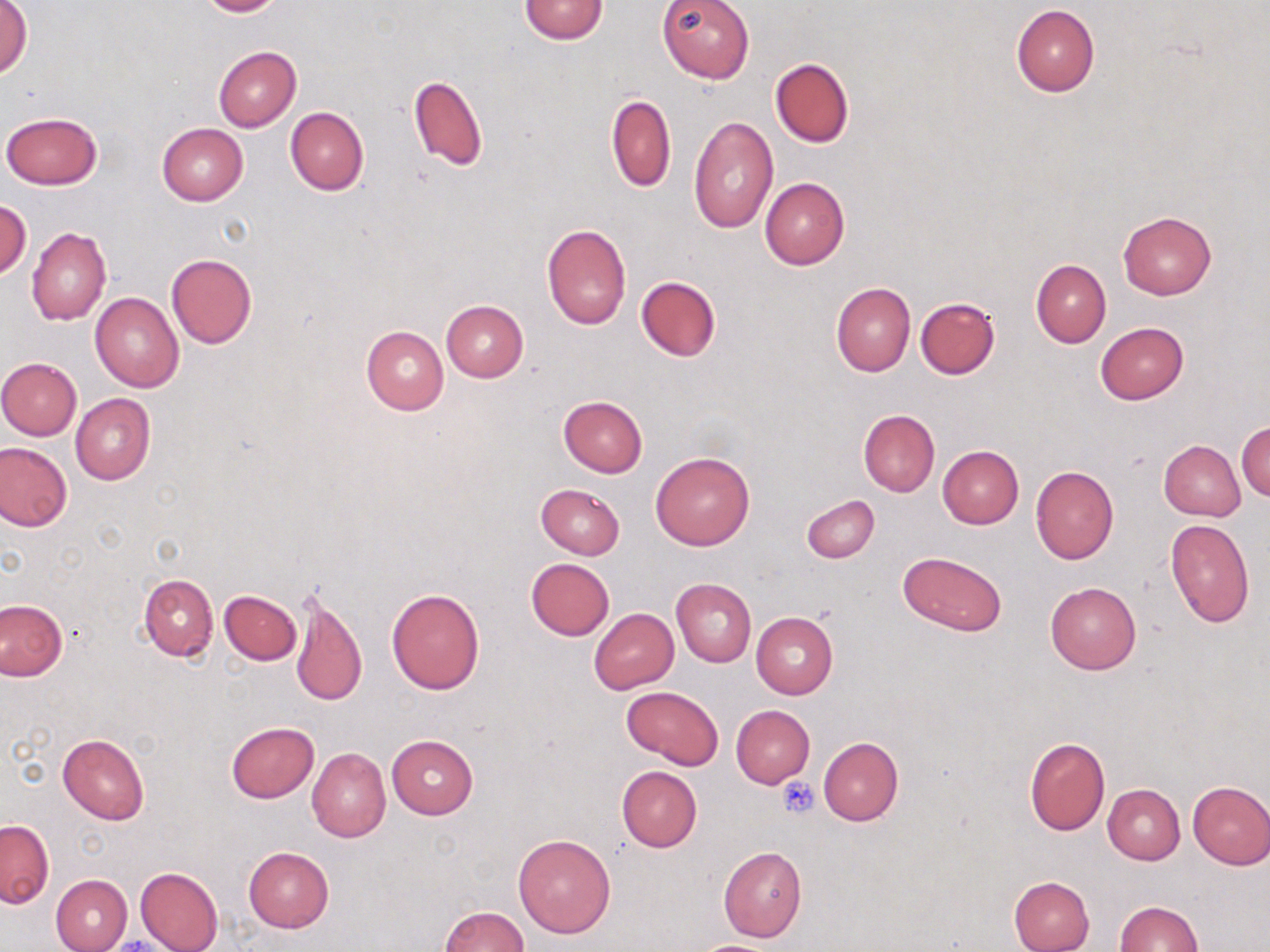
{
  "slide_level_diagnosis": "negative for blood parasites",
  "modality": "light microscopy",
  "magnification": "1000x",
  "image_size": "1270×952 pixels",
  "stain": "May-Grünwald-Giemsa",
  "preparation": "thin blood smear",
  "uninfected_red_blood_cell_locations": "approximate bounding boxes as [x1, y1, x2, y2] in pixels: [1, 0, 33, 80], [196, 0, 287, 17], [517, 0, 609, 43], [656, 0, 755, 83], [1010, 5, 1100, 96], [213, 47, 301, 131], [769, 58, 854, 147], [409, 76, 487, 171], [606, 94, 675, 192], [285, 107, 369, 195], [1, 112, 103, 189], [688, 116, 778, 233], [157, 122, 248, 206], [759, 178, 850, 270], [0, 200, 31, 280], [1119, 211, 1216, 299], [541, 224, 631, 330], [27, 227, 110, 325], [166, 252, 256, 349], [1031, 258, 1111, 348], [636, 275, 721, 361], [830, 282, 916, 376], [90, 293, 184, 392], [915, 297, 1000, 378], [440, 299, 529, 382], [1096, 321, 1188, 404], [360, 326, 449, 415], [0, 357, 81, 440], [71, 394, 155, 485], [558, 396, 648, 477], [858, 409, 940, 496], [1236, 421, 1270, 502], [1159, 440, 1245, 521], [1, 442, 71, 531], [937, 446, 1023, 529], [650, 452, 755, 550], [1030, 465, 1119, 564], [536, 483, 624, 558], [800, 495, 879, 564], [1165, 519, 1255, 628], [897, 551, 1007, 635], [526, 558, 614, 640], [139, 573, 217, 660], [672, 578, 756, 667], [1045, 583, 1141, 674], [386, 587, 486, 694], [219, 589, 302, 664], [289, 589, 368, 710], [0, 598, 67, 680], [589, 608, 678, 693], [751, 613, 838, 699], [622, 686, 724, 769], [731, 705, 815, 788], [226, 721, 319, 802], [58, 733, 148, 825], [387, 735, 477, 818], [818, 737, 903, 826], [1024, 738, 1111, 836], [307, 748, 391, 843], [616, 766, 702, 853], [1186, 782, 1270, 870], [1103, 783, 1185, 864], [0, 819, 52, 908], [513, 833, 616, 938], [243, 846, 333, 932], [718, 846, 808, 942], [135, 867, 223, 952], [51, 875, 132, 952], [1009, 876, 1095, 952], [1113, 901, 1203, 952], [439, 906, 527, 952], [688, 940, 787, 952]",
  "field_of_view": "one of a larger specimen",
  "platelet_locations": "approximate bounding boxes as [x1, y1, x2, y2] in pixels: [777, 776, 821, 819]"
}